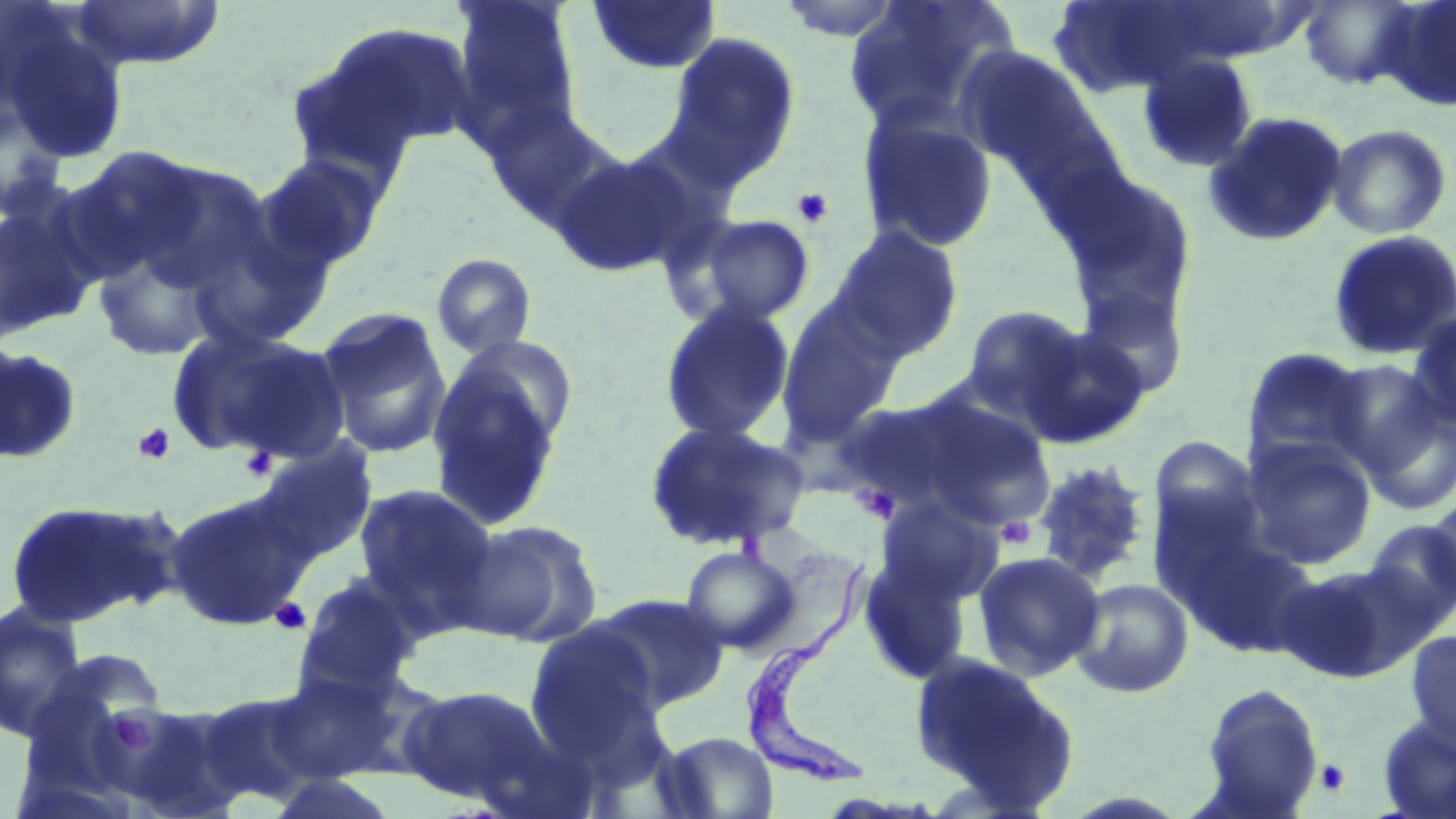
Approximate bounding boxes as [x1, y1, x2, y2] in pixels. Uninfected red blood cell locations: [68, 0, 227, 71], [586, 0, 722, 76], [774, 0, 907, 41], [843, 0, 1015, 136], [1298, 0, 1422, 91], [1381, 0, 1456, 111], [450, 1, 582, 147], [1049, 1, 1218, 98], [1, 10, 130, 164], [295, 21, 477, 172], [665, 31, 801, 186], [953, 45, 1095, 173], [1136, 53, 1258, 173], [484, 104, 620, 233], [0, 105, 66, 222], [857, 108, 1000, 254], [1203, 110, 1348, 247], [1325, 123, 1454, 240], [61, 146, 203, 281], [549, 148, 704, 278], [254, 153, 388, 274], [127, 159, 275, 298], [1051, 164, 1200, 329], [0, 194, 102, 342], [182, 207, 335, 353], [691, 214, 816, 325], [828, 224, 965, 360], [1326, 230, 1456, 361], [89, 236, 230, 363], [431, 253, 538, 359], [1074, 281, 1190, 401], [775, 299, 904, 445], [658, 301, 796, 443], [960, 305, 1090, 419], [316, 306, 453, 460], [1407, 310, 1456, 429], [1015, 324, 1150, 449], [165, 326, 347, 462], [0, 345, 83, 465], [1241, 346, 1373, 470], [1325, 358, 1446, 478], [425, 359, 567, 532], [848, 390, 1056, 533], [1361, 402, 1456, 517], [643, 420, 811, 552], [1148, 435, 1266, 559], [1241, 436, 1378, 570], [254, 440, 377, 564], [1030, 459, 1153, 585], [353, 484, 498, 620], [164, 493, 312, 631], [875, 495, 1004, 608], [1424, 496, 1456, 604], [3, 497, 183, 627], [458, 519, 604, 647], [1362, 519, 1456, 632], [1174, 527, 1322, 657], [681, 545, 802, 654], [973, 551, 1106, 680], [858, 552, 975, 686], [1274, 562, 1419, 683], [296, 573, 426, 694], [1069, 578, 1195, 699], [589, 592, 730, 714], [0, 602, 88, 741], [525, 620, 663, 761], [1404, 630, 1456, 750], [908, 651, 1078, 809], [27, 655, 167, 780], [265, 671, 405, 783], [1200, 683, 1324, 816], [398, 684, 549, 805], [192, 690, 328, 810], [112, 702, 247, 819], [1376, 717, 1456, 818], [657, 731, 779, 818]. Platelet locations: [791, 186, 835, 228], [133, 422, 177, 465], [239, 446, 277, 483], [851, 483, 900, 525], [996, 515, 1037, 549], [271, 598, 311, 635], [106, 711, 152, 756], [1315, 758, 1351, 796]. Trypanosoma brucei locations: [742, 554, 879, 789]. Slide-level diagnosis: Trypanosoma brucei. Optical microscopy. 1000x magnification. Image is 1456×819 pixels. May-Grünwald-Giemsa-stained preparation. One field of a larger specimen. Thin blood film.